Give the extent of all Plasmodium vivax-infected red blood cells.
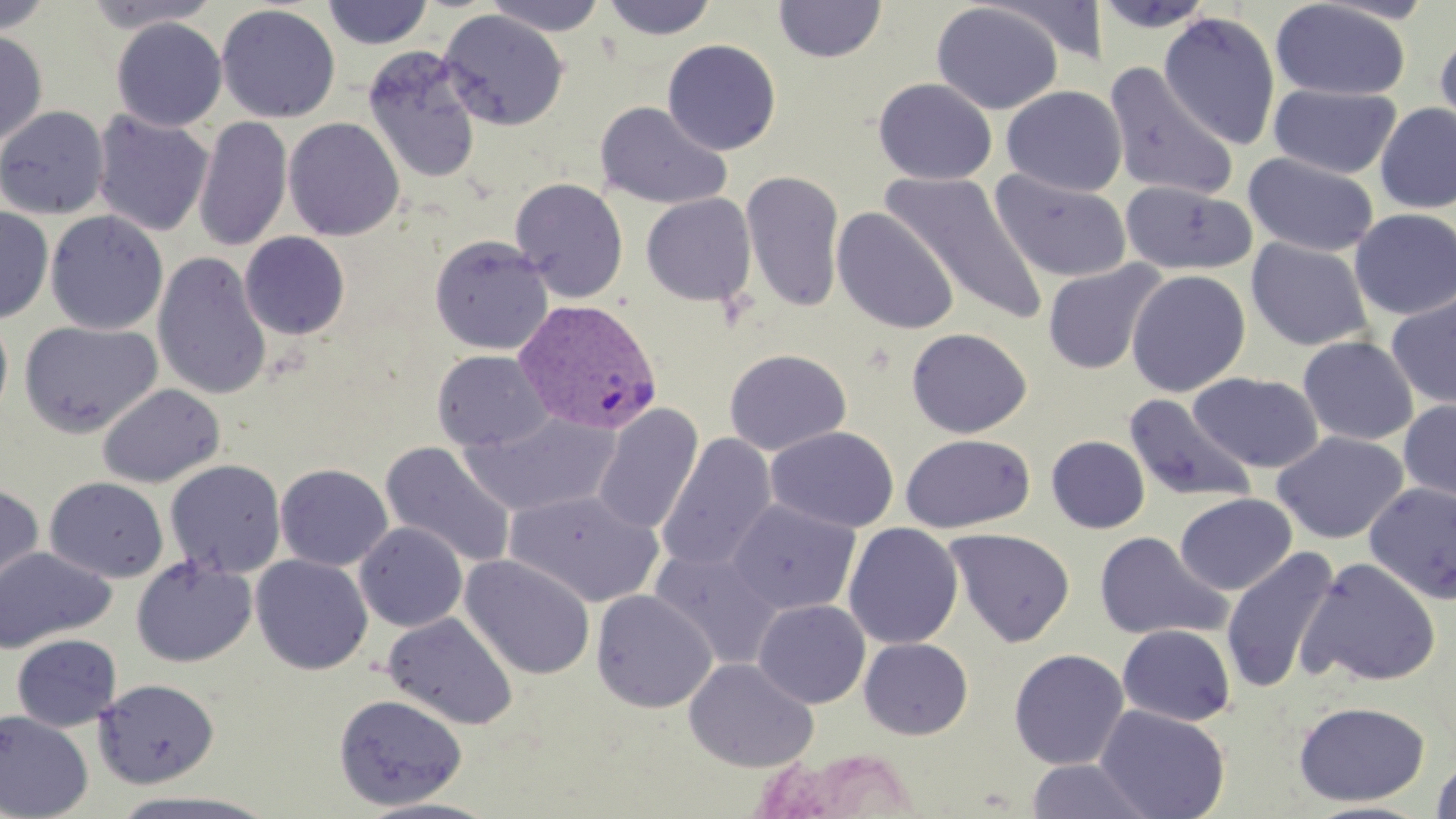

Approximate bounding boxes as (x1, y1, x2, y2) in pixels.
Plasmodium vivax-infected red blood cells: (514, 298, 663, 436).

Uninfected red blood cell locations: (0, 0, 56, 36), (83, 0, 222, 33), (321, 0, 434, 49), (483, 0, 609, 36), (601, 0, 718, 40), (773, 0, 887, 63), (1093, 0, 1217, 34), (1271, 0, 1411, 101), (931, 2, 1064, 115), (216, 4, 340, 123), (437, 9, 569, 131), (1158, 11, 1281, 149), (111, 17, 228, 132), (1434, 26, 1456, 145), (0, 29, 47, 148), (662, 39, 781, 155), (361, 46, 484, 185), (1103, 62, 1239, 201), (873, 77, 997, 184), (1268, 83, 1401, 179), (1001, 85, 1127, 197), (595, 101, 731, 209), (1374, 103, 1456, 213), (0, 105, 109, 219), (91, 109, 215, 238), (194, 115, 293, 252), (283, 117, 404, 241), (1243, 152, 1380, 257), (989, 169, 1132, 283), (882, 170, 1047, 323), (741, 171, 845, 312), (510, 178, 628, 303), (1120, 180, 1255, 276), (641, 193, 757, 307), (0, 206, 53, 323), (831, 207, 960, 335), (1350, 208, 1456, 320), (45, 210, 168, 335), (240, 232, 350, 340), (429, 234, 554, 355), (1246, 238, 1373, 352), (152, 252, 272, 400), (1042, 261, 1166, 374), (1126, 269, 1251, 397), (1386, 292, 1456, 410), (0, 312, 13, 423), (18, 321, 163, 438), (906, 327, 1032, 438), (1298, 335, 1418, 446), (724, 348, 851, 456), (432, 349, 551, 451), (1188, 372, 1324, 473), (97, 383, 225, 488), (1124, 392, 1257, 506), (1397, 398, 1456, 507), (592, 404, 704, 535), (460, 411, 621, 518), (765, 425, 900, 533), (1273, 432, 1408, 543), (656, 433, 777, 574), (899, 433, 1035, 534), (1046, 436, 1150, 533), (380, 441, 517, 569), (164, 459, 286, 578), (275, 463, 393, 571), (44, 476, 169, 583), (0, 482, 44, 604), (1364, 482, 1456, 605), (505, 489, 664, 608), (1175, 492, 1296, 595), (728, 498, 861, 616), (355, 522, 468, 632), (843, 522, 963, 649), (945, 527, 1075, 647), (1094, 531, 1230, 642), (353, 533, 568, 650), (0, 545, 116, 654), (1221, 546, 1340, 695), (649, 547, 783, 669), (250, 554, 373, 675), (459, 554, 596, 680), (131, 556, 257, 667), (1298, 556, 1441, 688), (591, 589, 717, 712), (753, 599, 870, 709), (383, 612, 519, 730), (1117, 624, 1236, 726), (11, 633, 122, 731), (858, 638, 973, 740), (1008, 648, 1129, 770), (683, 657, 818, 773), (94, 678, 219, 788), (333, 693, 468, 811), (1293, 700, 1430, 806), (1095, 705, 1231, 819), (0, 710, 94, 819), (1429, 756, 1456, 819), (1025, 758, 1155, 818), (107, 789, 279, 818), (351, 797, 504, 819). Slide-level diagnosis: Plasmodium vivax. One field of a larger specimen. 1000x magnification. May-Grünwald-Giemsa stain. Thin blood smear. Light microscopy. Image is 1456×819 pixels.